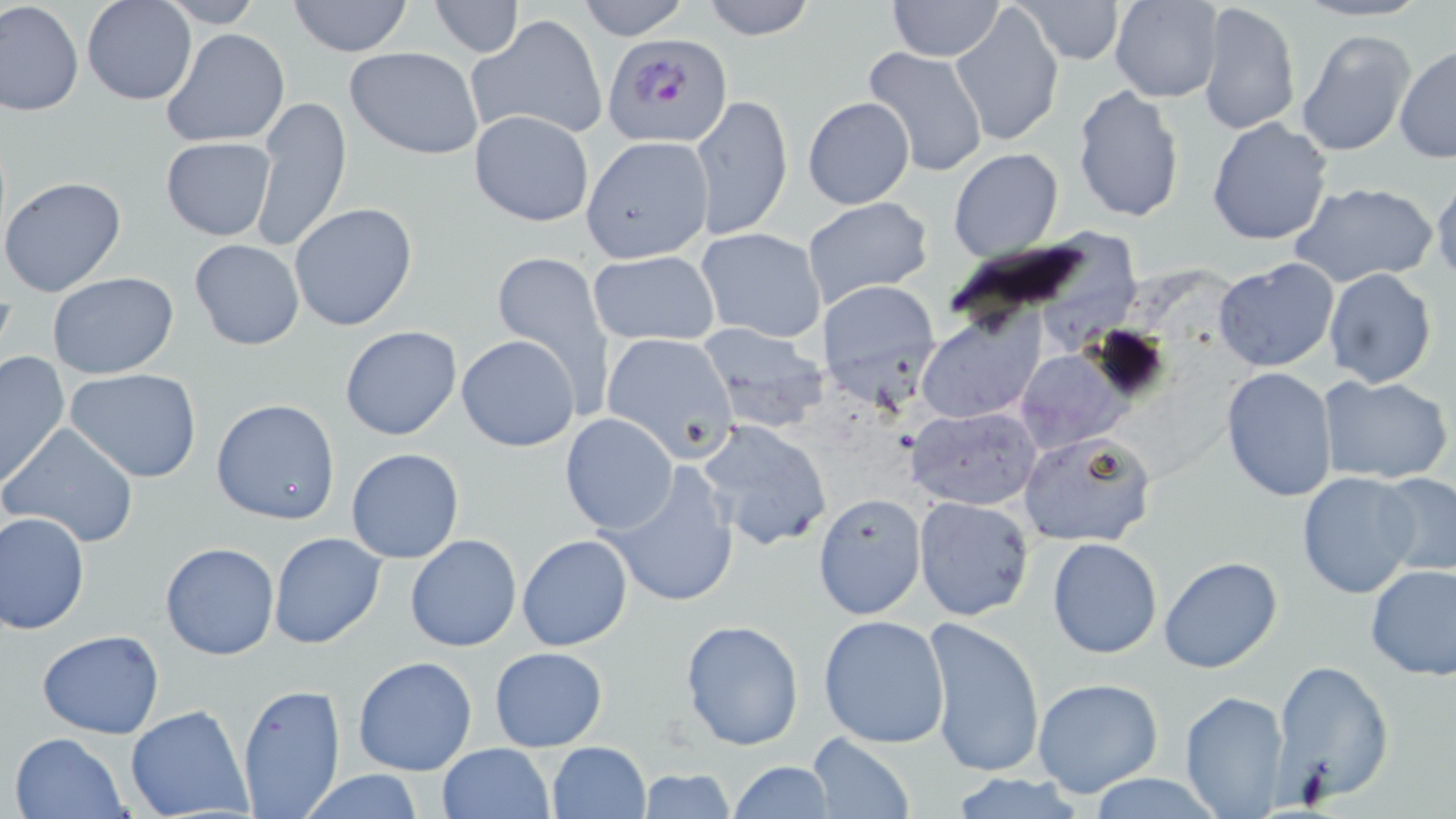

Approximate bounding boxes as (x1, y1, x2, y2) in pixels. Plasmodium falciparum-infected red blood cell locations: (603, 32, 733, 146). Uninfected red blood cell locations: (82, 0, 197, 105), (285, 0, 416, 56), (575, 0, 692, 40), (697, 0, 819, 39), (886, 0, 1004, 60), (1014, 0, 1126, 67), (1110, 0, 1223, 103), (1, 1, 83, 116), (158, 1, 270, 28), (951, 1, 1066, 146), (1196, 1, 1300, 139), (429, 2, 522, 57), (1091, 7, 1208, 187), (467, 15, 608, 141), (161, 27, 291, 149), (1294, 28, 1417, 158), (344, 46, 484, 161), (1394, 46, 1456, 163), (861, 47, 990, 178), (1072, 84, 1185, 224), (691, 93, 793, 240), (251, 96, 352, 254), (802, 98, 916, 209), (468, 109, 595, 228), (1206, 117, 1333, 247), (161, 136, 277, 241), (582, 136, 713, 265), (948, 149, 1064, 262), (1430, 174, 1456, 283), (0, 175, 126, 298), (1292, 181, 1439, 291), (801, 197, 934, 311), (288, 202, 418, 331), (1044, 224, 1141, 347), (695, 227, 827, 344), (188, 237, 305, 351), (588, 249, 719, 346), (487, 250, 616, 415), (1213, 259, 1339, 373), (1322, 268, 1437, 389), (46, 272, 181, 381), (816, 280, 940, 404), (916, 309, 1047, 423), (696, 320, 831, 430), (339, 325, 463, 441), (601, 330, 739, 463), (455, 334, 580, 452), (1014, 349, 1126, 451), (1, 351, 71, 488), (64, 367, 203, 484), (1221, 367, 1337, 503), (1317, 375, 1452, 484), (212, 398, 341, 525), (905, 405, 1042, 510), (559, 413, 680, 535), (697, 419, 832, 549), (2, 423, 141, 550), (1018, 431, 1158, 549), (345, 448, 465, 563), (602, 460, 741, 608), (1296, 471, 1422, 597), (1374, 472, 1456, 578), (812, 495, 925, 621), (913, 496, 1035, 620), (0, 510, 89, 634), (268, 531, 387, 649), (405, 534, 522, 651), (517, 535, 633, 651), (1047, 537, 1162, 658), (159, 541, 280, 661), (1159, 556, 1284, 674), (1365, 563, 1456, 679), (818, 614, 950, 746), (924, 618, 1045, 778), (680, 619, 804, 751), (37, 630, 165, 739), (489, 646, 606, 750), (352, 655, 478, 777), (1271, 658, 1395, 804), (1031, 677, 1164, 800), (235, 681, 347, 818), (1177, 689, 1292, 818), (125, 704, 254, 819), (8, 731, 129, 819), (805, 732, 914, 818), (547, 741, 651, 819), (437, 742, 555, 819), (727, 760, 834, 818), (637, 767, 737, 819), (294, 768, 429, 819), (1086, 774, 1223, 817). Slide-level diagnosis: Plasmodium falciparum. Captured at 1000x magnification. Thin blood smear. Single field of view. Light microscopy. Image is 1456×819 pixels. May-Grünwald-Giemsa-stained preparation.